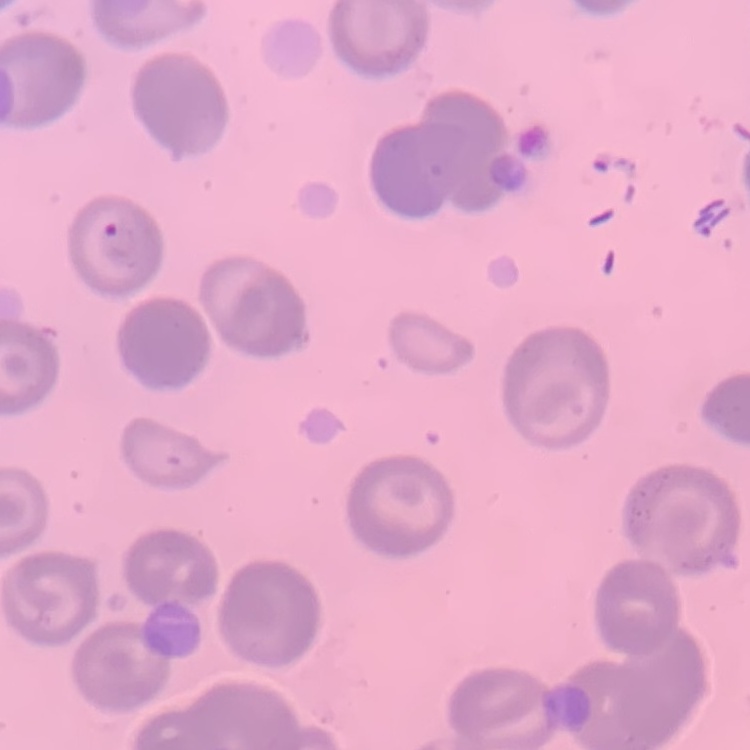
Summary:
  - Red blood cell morphology: no rouleaux formation
  - Stain: Field's or Giemsa
  - Image type: square crop of a larger photomicrograph
  - Preparation: thin peripheral smear